Assess the morphology of the red blood cells.
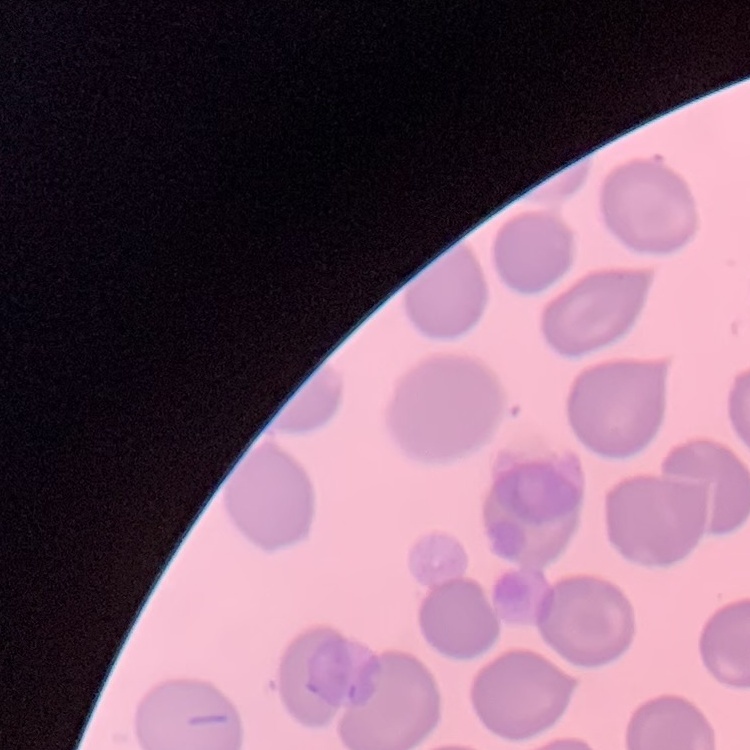
No rouleaux formation.

Summary:
  - Stain: Field's or Giemsa
  - Preparation: thin peripheral smear
  - Image type: square crop of a larger photomicrograph